Assess the morphology of the red blood cells.
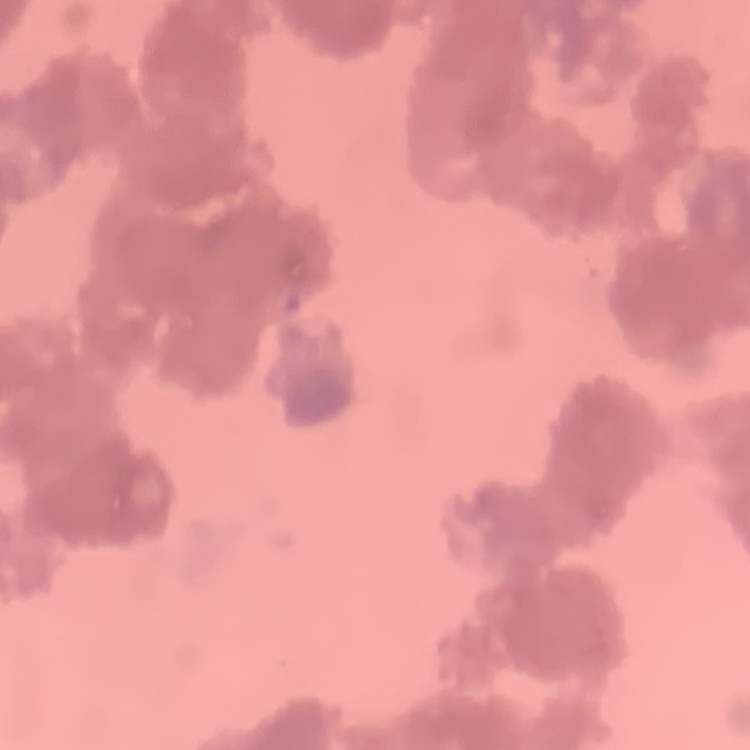

They show rouleaux formation.

Square crop of a larger photomicrograph. Thin blood smear. Stained with either Field's or Giemsa.